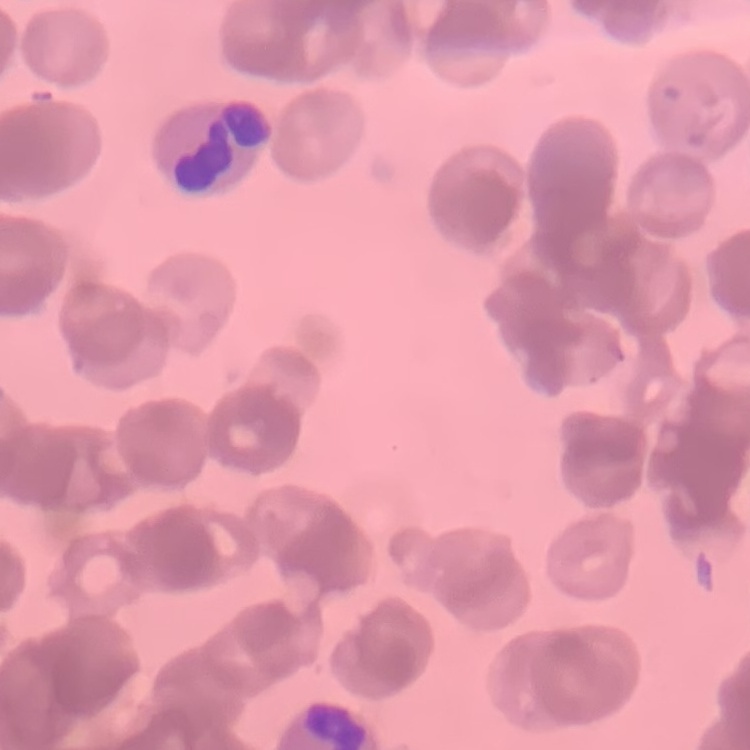
{
  "red_blood_cell_morphology": "rouleaux formation",
  "image_type": "one tile cut from a larger photomicrograph",
  "stain": "Field's or Giemsa",
  "preparation": "thin peripheral smear"
}